Point out each malaria parasite and each leukocyte.
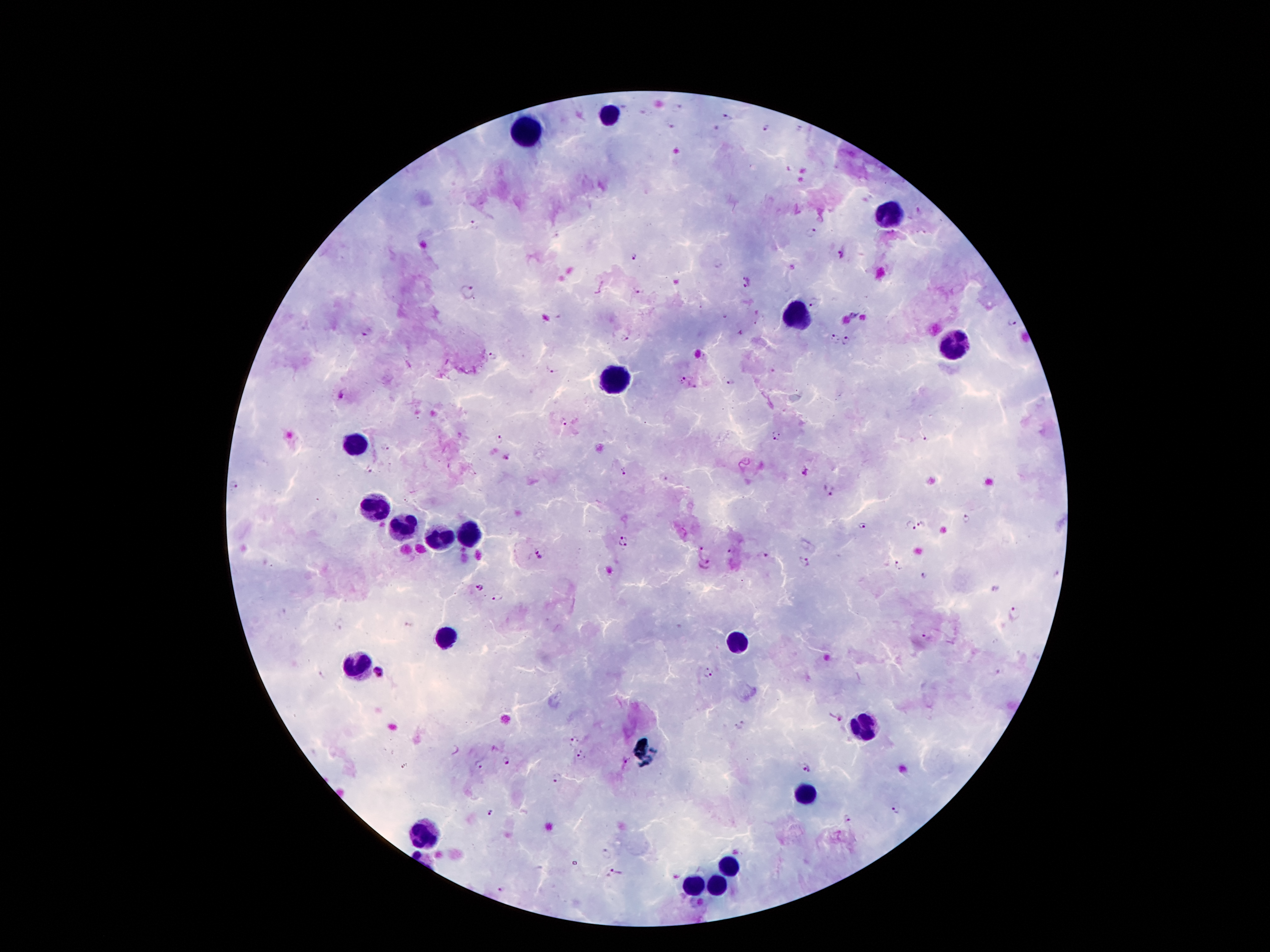

Approximate centers as {x, y} in pixels.
Malaria parasites: {728, 116}, {670, 125}, {764, 126}, {799, 129}, {474, 224}, {813, 232}, {842, 252}, {633, 256}, {794, 266}, {748, 282}, {639, 291}, {467, 292}, {812, 301}, {1012, 322}, {741, 330}, {366, 333}, {626, 337}, {834, 339}, {848, 342}, {494, 357}, {551, 368}, {773, 371}, {682, 381}, {729, 381}, {340, 394}, {564, 421}, {775, 435}, {925, 438}, {497, 440}, {383, 448}, {506, 456}, {369, 471}, {622, 471}, {807, 474}, {664, 478}, {233, 486}, {830, 491}, {967, 518}, {924, 524}, {862, 526}, {912, 526}, {624, 540}, {700, 549}, {731, 551}, {539, 553}, {764, 555}, {803, 560}, {705, 563}, {900, 565}, {1056, 573}, {924, 575}, {479, 587}, {497, 597}, {1015, 612}, {408, 625}, {926, 637}, {1000, 671}, {379, 672}, {708, 673}, {322, 674}, {840, 717}, {739, 724}, {576, 739}, {581, 756}, {506, 760}, {478, 766}, {807, 768}, {557, 778}, {897, 808}, {492, 813}, {847, 818}, {607, 855}, {614, 873}, {502, 890}, {702, 903}.
Leukocytes: {609, 116}, {527, 132}, {890, 216}, {799, 316}, {953, 347}, {613, 378}, {355, 444}, {376, 506}, {403, 526}, {465, 535}, {439, 539}, {445, 639}, {737, 641}, {359, 663}, {863, 727}, {805, 791}, {427, 835}, {726, 866}, {691, 886}, {717, 886}.

magnification = 100x
capture = smartphone camera through the microscope eyepiece
field of view = single
patient malaria status = positive for Plasmodium falciparum
preparation = thick peripheral-blood smear
image size = 1270×952 pixels
stain = Giemsa